Locate and identify every blood parasite.
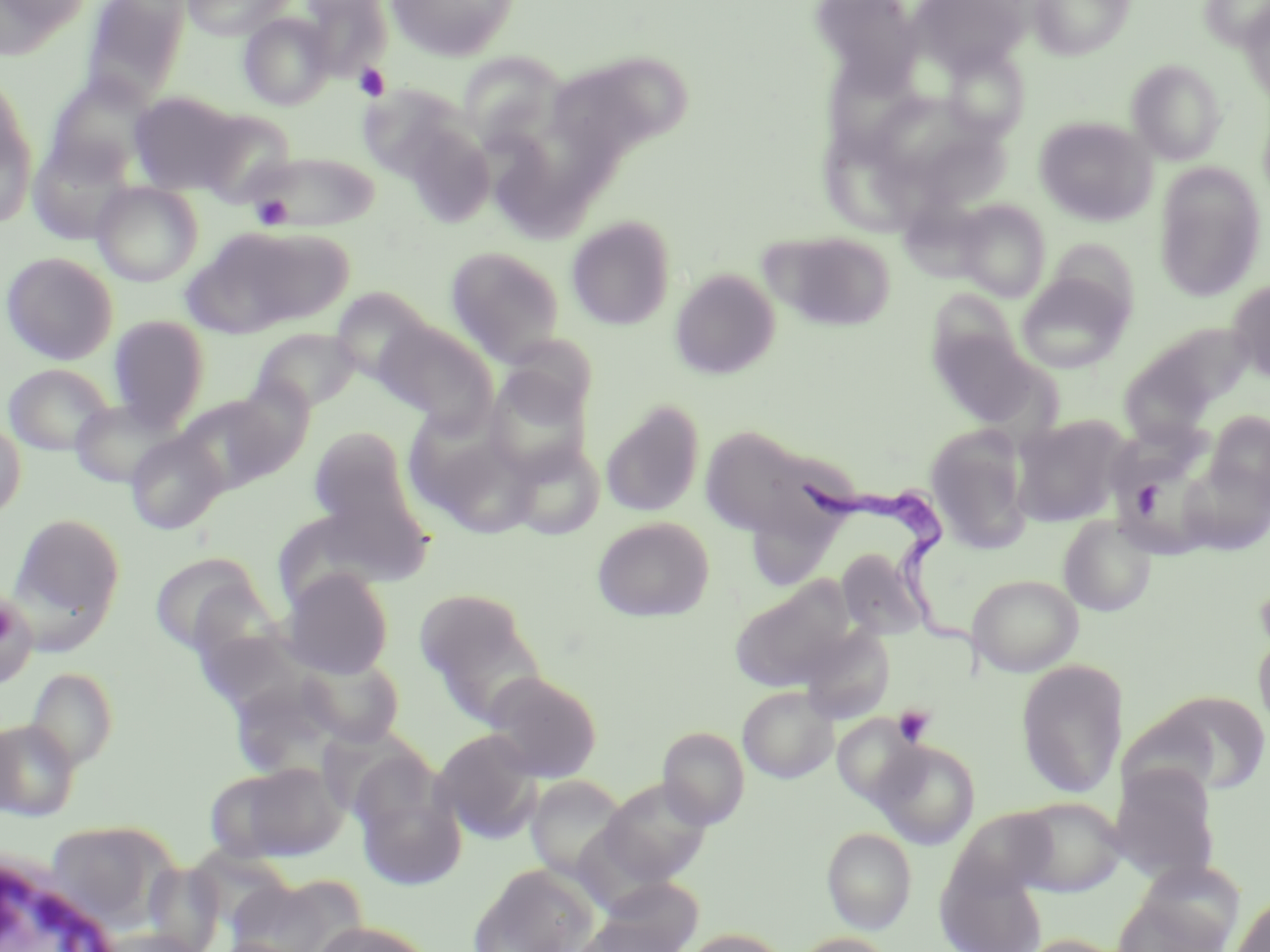

Approximate bounding boxes as (x1,y1)-(x2,y2) corner pairs in pixels.
Trypanosoma brucei: (807,474)-(988,676).
No Plasmodium falciparum, Plasmodium ovale, Plasmodium malariae, Plasmodium vivax, or Babesia divergens observed.

slide-level diagnosis = Trypanosoma brucei
platelet locations = approximate bounding boxes as (x1,y1)-(x2,y2) corner pairs in pixels: (353,63)-(391,101), (251,195)-(292,229), (893,705)-(935,746)
modality = light microscopy
stain = May-Grünwald-Giemsa
uninfected red blood cell locations = approximate bounding boxes as (x1,y1)-(x2,y2) corner pairs in pixels: (0,0)-(90,56), (81,0)-(192,105), (180,0)-(292,40), (300,0)-(392,80), (386,0)-(519,61), (912,0)-(1030,75), (1029,0)-(1135,59), (1199,1)-(1270,51), (1240,2)-(1270,106), (239,13)-(336,110), (942,46)-(1030,140), (458,52)-(561,147), (549,52)-(690,169), (824,54)-(928,167), (1126,60)-(1226,165), (44,73)-(155,181), (358,84)-(467,183), (129,92)-(246,195), (873,94)-(988,181), (0,97)-(37,230), (194,109)-(297,205), (1035,117)-(1156,226), (404,125)-(495,227), (27,137)-(137,244), (821,140)-(922,243), (497,144)-(610,241), (241,151)-(382,232), (1153,163)-(1265,301), (91,181)-(203,286), (955,199)-(1051,302), (566,216)-(675,330), (185,226)-(350,336), (768,232)-(896,332), (1042,238)-(1141,321), (444,246)-(566,365), (1,251)-(118,365), (670,268)-(780,379), (1016,274)-(1132,373), (1228,280)-(1270,384), (329,287)-(432,383), (929,290)-(1023,377), (107,315)-(210,430), (375,319)-(495,427), (929,322)-(1045,428), (252,327)-(362,412), (1120,356)-(1219,451), (4,363)-(114,455), (485,372)-(592,481), (173,393)-(291,492), (70,399)-(181,489), (600,401)-(705,518), (1204,412)-(1270,508), (1010,415)-(1131,527), (0,417)-(26,520), (412,424)-(541,538), (307,425)-(419,534), (700,425)-(816,537), (925,425)-(1034,554), (125,432)-(226,534), (1112,435)-(1221,556), (509,441)-(604,541), (1177,456)-(1270,556), (11,513)-(125,632), (1058,514)-(1157,616), (591,517)-(714,622), (836,547)-(929,641), (148,553)-(273,658), (280,568)-(394,678), (968,573)-(1083,676), (732,578)-(856,691), (0,590)-(38,688), (415,590)-(545,725), (800,626)-(895,724), (1252,626)-(1270,739), (200,628)-(314,709), (300,654)-(404,747), (1016,660)-(1127,798), (24,666)-(119,769), (484,671)-(603,783), (738,686)-(838,783), (1142,690)-(1270,797), (832,714)-(925,806), (0,718)-(82,820), (657,727)-(750,829), (433,729)-(544,843), (872,740)-(981,849), (209,761)-(348,863), (1108,764)-(1221,885), (352,768)-(468,891), (525,775)-(630,883), (598,777)-(712,886), (1013,796)-(1126,897), (42,821)-(173,927), (822,827)-(917,934), (469,865)-(599,952), (937,867)-(1047,952), (226,873)-(365,952), (595,877)-(706,950), (1113,887)-(1231,952), (1232,893)-(1270,952), (309,921)-(438,952), (91,928)-(212,952), (680,929)-(792,952), (790,933)-(897,952), (1017,934)-(1134,952)
white blood cell locations = approximate bounding boxes as (x1,y1)-(x2,y2) corner pairs in pixels: (1,851)-(126,952)
preparation = thin blood film
image size = 1270×952 pixels
field of view = single
magnification = 1000x